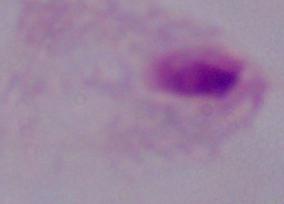

{
  "identification": "trichomonad",
  "modality": "micrograph",
  "magnification": "1000x"
}